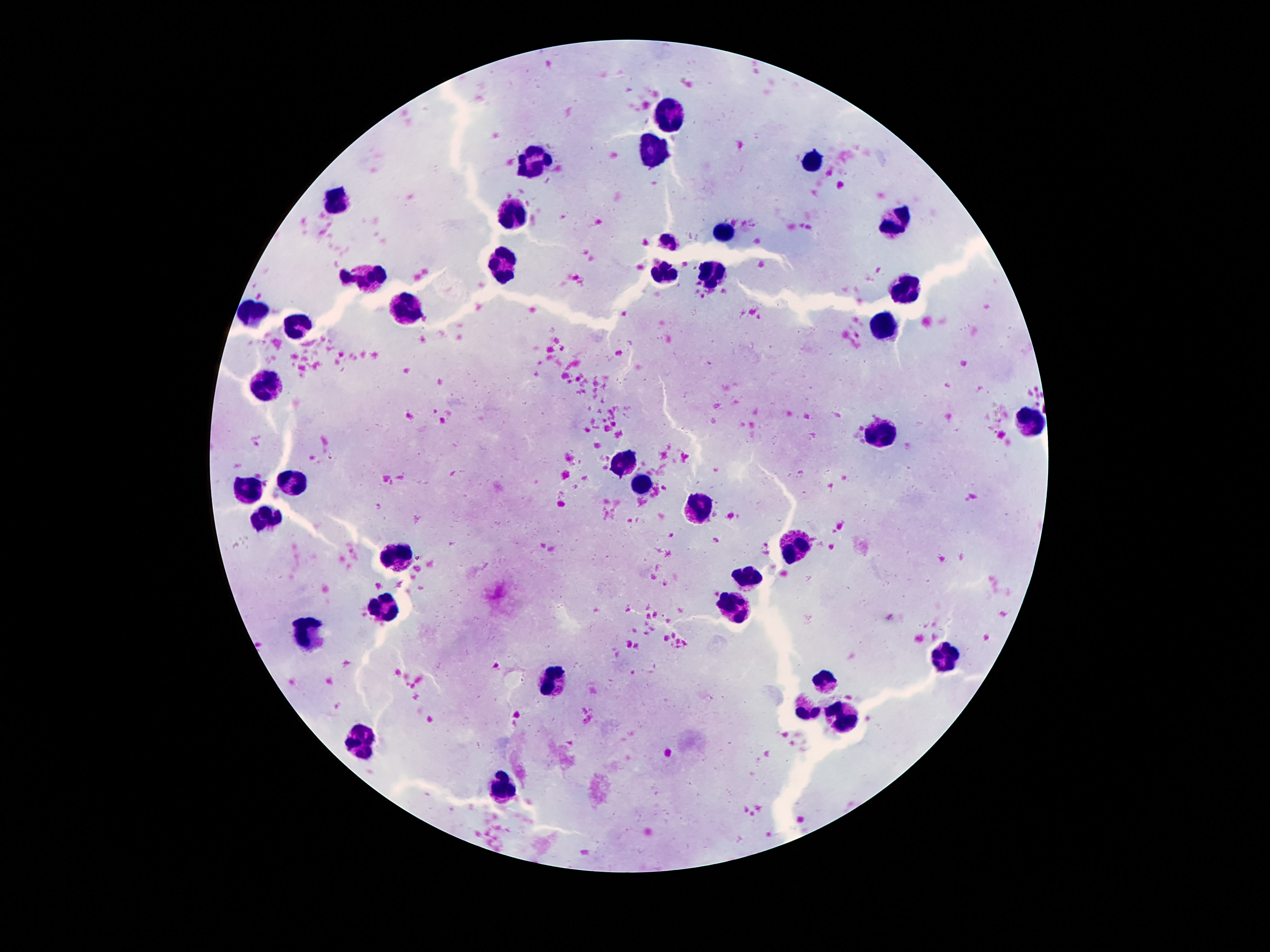

Approximate centers as (x, y) in pixels.
Summary:
  - Leukocyte locations: (671, 113), (656, 148), (532, 159), (812, 159), (340, 196), (512, 210), (903, 214), (726, 229), (505, 267), (711, 271), (366, 273), (661, 273), (905, 289), (404, 307), (253, 311), (883, 325), (298, 329), (269, 387), (1031, 422), (883, 437), (629, 462), (293, 481), (643, 482), (251, 490), (698, 507), (271, 520), (797, 542), (401, 556), (744, 576), (386, 602), (737, 611), (307, 630), (945, 658), (550, 678), (828, 680), (809, 709), (846, 717), (362, 742), (501, 788)
  - Patient malaria status: negative
  - Image size: 1270×952 pixels
  - Field of view: single
  - Capture: smartphone camera through the microscope eyepiece
  - Stain: Giemsa
  - Magnification: 100x
  - Preparation: thick blood smear